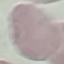 Malaria status: uninfected. Cell patch, automatically extracted from a larger field of view and resized to 64 × 64 pixels. Giemsa-stained preparation. Thin blood film. Acquired by smartphone through the microscope eyepiece.